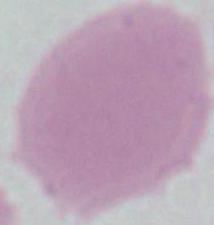
magnification = 1000x
modality = photomicrograph
identification = red blood cell